Identify the cell.
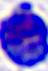

This is a leukocyte.

Summary:
  - Magnification: 400x
  - Modality: micrograph